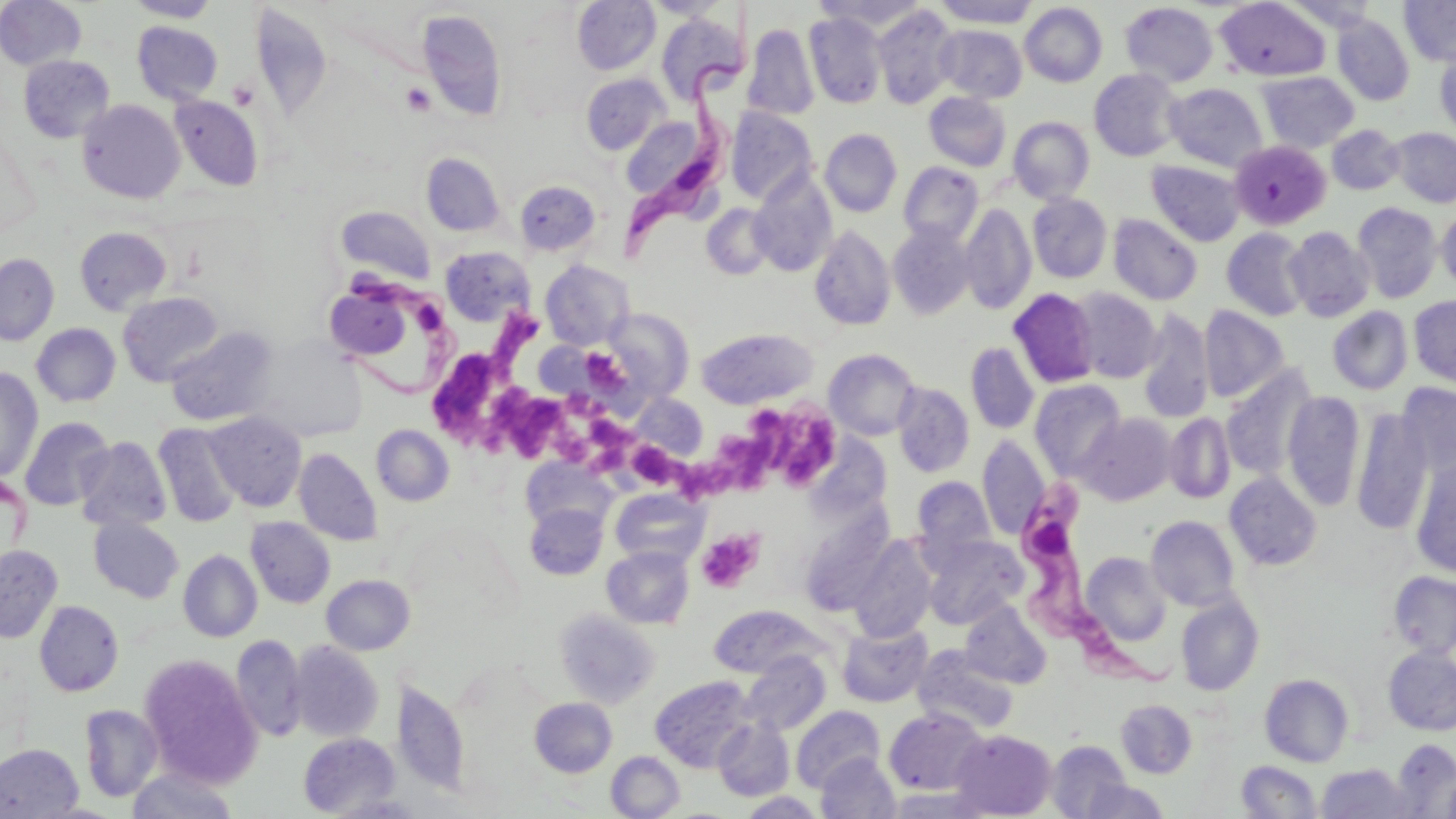
slide_level_diagnosis: Trypanosoma brucei
image_size: 1456×819 pixels
stain: May-Grünwald-Giemsa
field_of_view: one of a larger specimen
magnification: 1000x
uninfected_red_blood_cell_locations: 'approximate bounding boxes as [x1, y1, x2, y2] in pixels: [0, 0, 87, 70], [124, 0, 221, 22], [642, 0, 731, 20], [934, 0, 1039, 27], [1399, 0, 1456, 66], [572, 1, 661, 74], [1215, 1, 1330, 82], [1120, 2, 1218, 87], [1280, 2, 1385, 31], [1020, 3, 1107, 87], [8, 4, 101, 131], [872, 5, 960, 108], [418, 9, 507, 121], [804, 12, 886, 109], [656, 13, 747, 104], [1333, 16, 1414, 105], [132, 21, 223, 105], [744, 23, 819, 121], [935, 25, 1027, 102], [1434, 49, 1456, 137], [19, 55, 115, 142], [1089, 69, 1183, 162], [1257, 71, 1359, 153], [581, 74, 669, 155], [1165, 83, 1268, 172], [924, 92, 1011, 171], [169, 95, 263, 191], [77, 99, 184, 203], [726, 107, 818, 205], [626, 117, 698, 202], [1009, 117, 1095, 203], [1327, 125, 1405, 195], [1390, 128, 1456, 207], [820, 129, 902, 217], [1229, 140, 1332, 230], [421, 152, 505, 236], [1146, 159, 1245, 246], [898, 162, 984, 246], [749, 171, 837, 277], [515, 180, 601, 256], [1027, 193, 1112, 283], [959, 203, 1037, 315], [1352, 203, 1442, 303], [702, 204, 775, 279], [337, 206, 435, 282], [1437, 208, 1456, 291], [1108, 214, 1203, 305], [887, 222, 976, 320], [74, 226, 171, 315], [809, 226, 895, 330], [1284, 226, 1374, 322], [1222, 228, 1311, 320], [440, 247, 532, 325], [0, 254, 59, 345], [541, 260, 631, 349], [1068, 287, 1162, 383], [1008, 288, 1100, 388], [330, 291, 418, 365], [118, 292, 223, 387], [1408, 296, 1456, 388], [1199, 305, 1290, 403], [1328, 306, 1413, 395], [599, 308, 694, 405], [1137, 310, 1214, 424], [31, 323, 120, 407], [166, 326, 278, 426], [696, 328, 817, 409], [965, 342, 1039, 434], [823, 348, 921, 440], [1220, 366, 1317, 481], [0, 367, 43, 482], [1030, 379, 1127, 480], [1397, 382, 1456, 479], [892, 383, 974, 477], [1282, 390, 1365, 511], [631, 393, 708, 460], [1351, 407, 1433, 535], [204, 412, 306, 511], [1077, 413, 1175, 505], [1164, 413, 1235, 504], [19, 417, 114, 511], [154, 423, 243, 528], [371, 425, 454, 506], [977, 436, 1049, 539], [75, 437, 171, 532], [294, 448, 382, 546], [521, 458, 615, 535], [1410, 458, 1456, 577], [1224, 472, 1322, 570], [913, 476, 995, 559], [610, 487, 709, 567], [525, 503, 608, 580], [795, 504, 896, 617], [1146, 515, 1241, 611], [245, 517, 335, 608], [89, 518, 184, 603], [922, 534, 1027, 629], [847, 535, 938, 643], [0, 544, 62, 643], [602, 546, 694, 629], [178, 549, 262, 642], [1080, 552, 1172, 646], [1388, 571, 1456, 658], [322, 575, 415, 655], [1175, 595, 1264, 696], [959, 600, 1052, 689], [34, 601, 123, 697], [709, 605, 828, 678], [554, 609, 660, 708], [837, 623, 932, 707], [231, 635, 307, 742], [288, 641, 384, 742], [913, 646, 1019, 735], [1383, 647, 1456, 735], [741, 653, 831, 735], [138, 654, 262, 789], [1260, 673, 1354, 767], [651, 676, 755, 771], [393, 678, 469, 795], [529, 697, 617, 777], [1116, 700, 1197, 777], [79, 705, 163, 802], [791, 705, 886, 792], [885, 709, 987, 795], [713, 718, 794, 800], [950, 729, 1057, 818], [298, 732, 400, 816], [1393, 739, 1456, 816], [1046, 740, 1134, 819], [0, 743, 83, 818], [606, 751, 685, 818], [816, 753, 900, 819], [1237, 760, 1322, 818], [1316, 764, 1414, 818], [126, 766, 239, 818], [1081, 776, 1168, 819], [884, 788, 987, 818], [739, 791, 825, 818], [328, 795, 429, 818]'
modality: optical microscopy
platelet_locations: 'approximate bounding boxes as [x1, y1, x2, y2] in pixels: [401, 82, 436, 116], [495, 308, 543, 371], [580, 347, 625, 392], [434, 352, 500, 432], [495, 387, 566, 458], [739, 405, 799, 470], [580, 409, 639, 456], [783, 412, 845, 491], [713, 431, 764, 494], [635, 447, 685, 487], [678, 456, 724, 509], [697, 529, 763, 594]'
trypanosoma_brucei_locations: 'approximate bounding boxes as [x1, y1, x2, y2] in pixels: [617, 14, 761, 269], [334, 266, 464, 395], [1018, 474, 1169, 684]'
preparation: thin blood smear